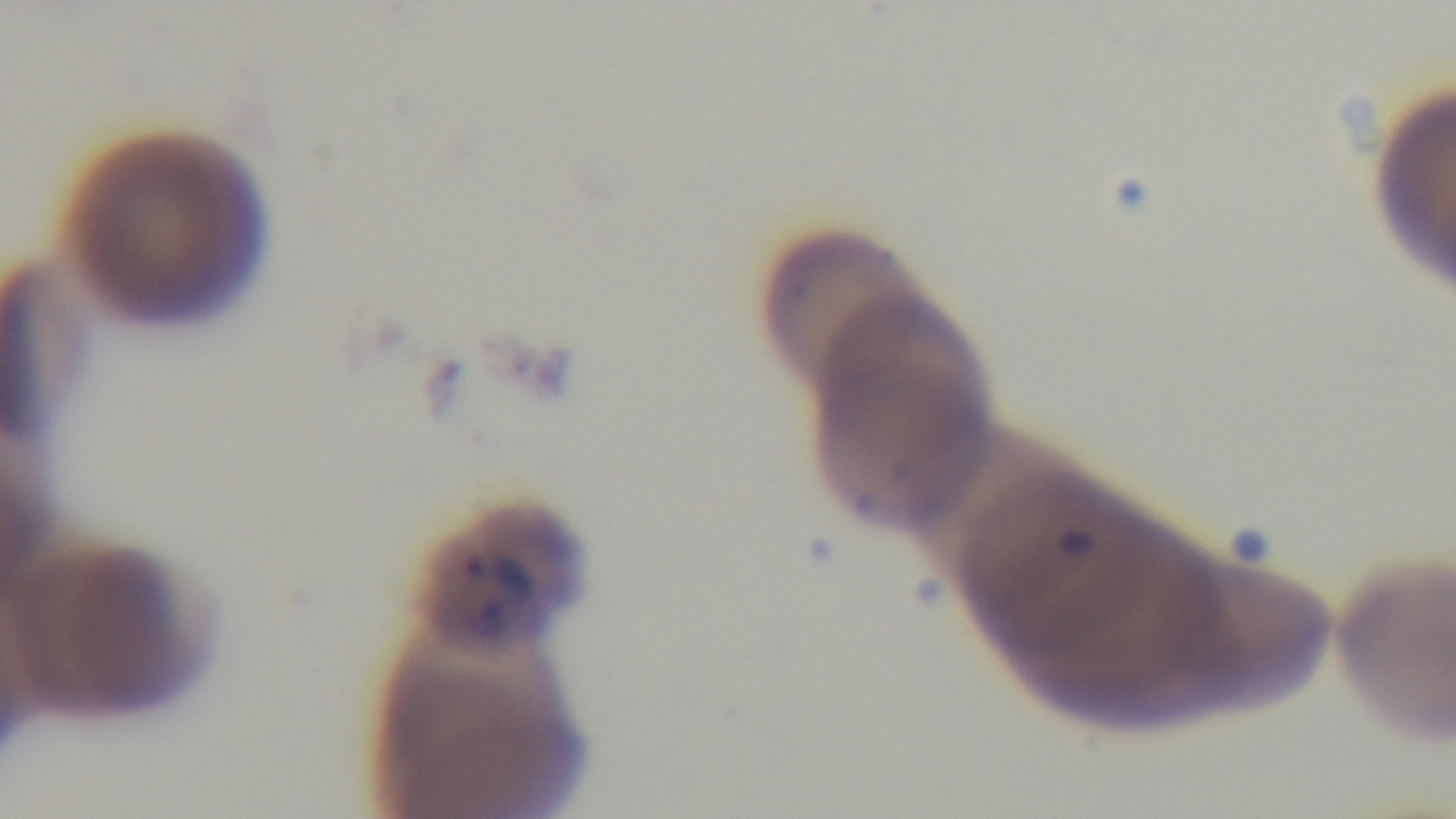
One field from the slide. Photomicrograph. Mounted 4K digital camera. Preparation: thin. 100x oil-immersion objective. Malaria status: positive. Giemsa stain.